Assess this cell for malaria.
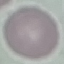

Uninfected.

capture: smartphone through the microscope eyepiece
stain: Giemsa
image_type: cell patch, automatically extracted from a larger field of view and resized to 64 × 64 pixels
preparation: thin blood film